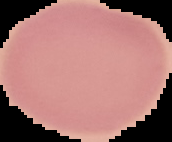

{
  "image_type": "segmented cell region on a black background",
  "image_size": "172×142 pixels",
  "preparation": "thin blood film",
  "result": "negative for malaria parasites"
}